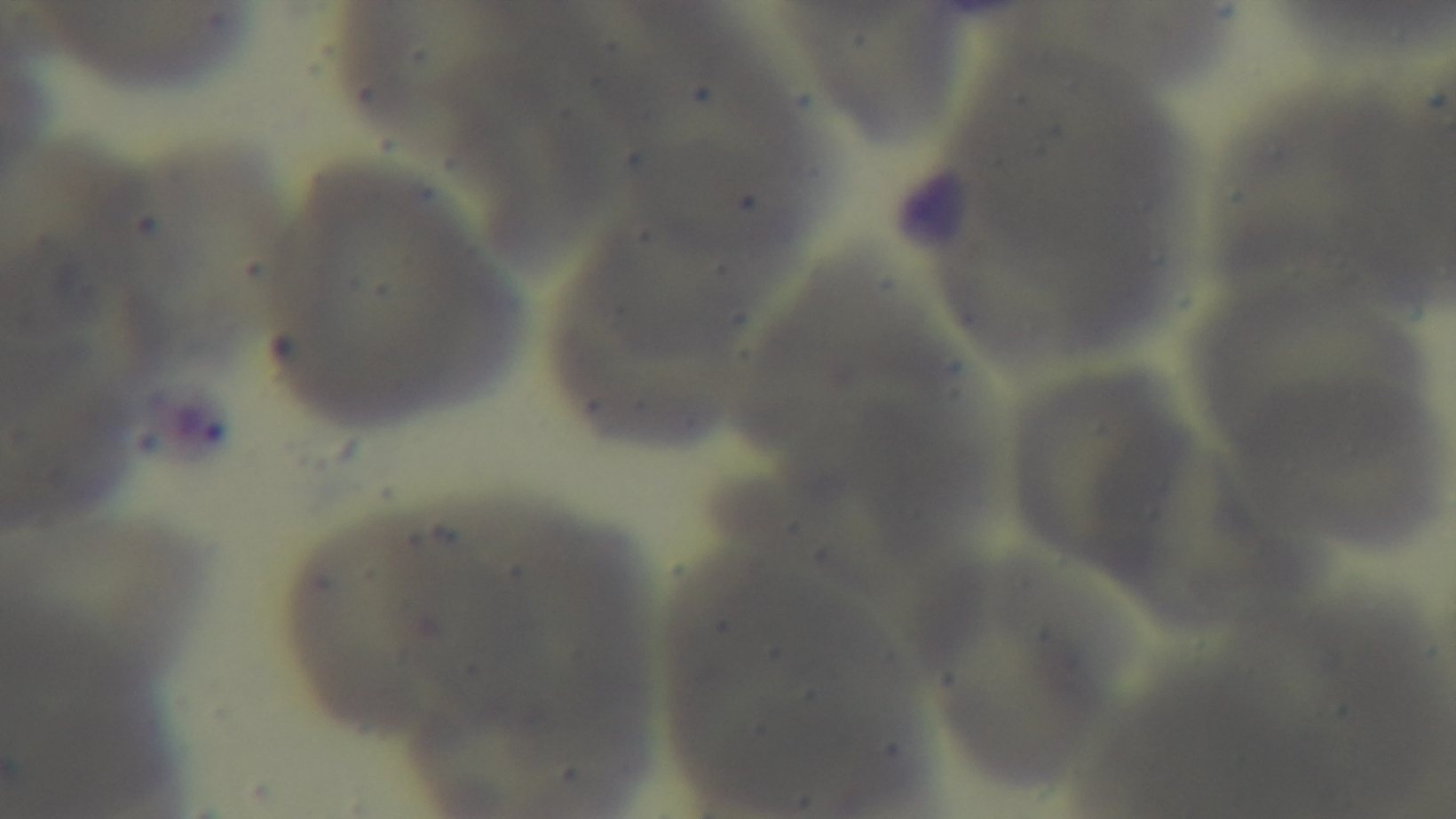
stain = Giemsa
preparation = thin blood film
objective = 100x oil immersion
modality = light microscopy
field of view = single
capture = mounted 4K digital camera
malaria status = negative